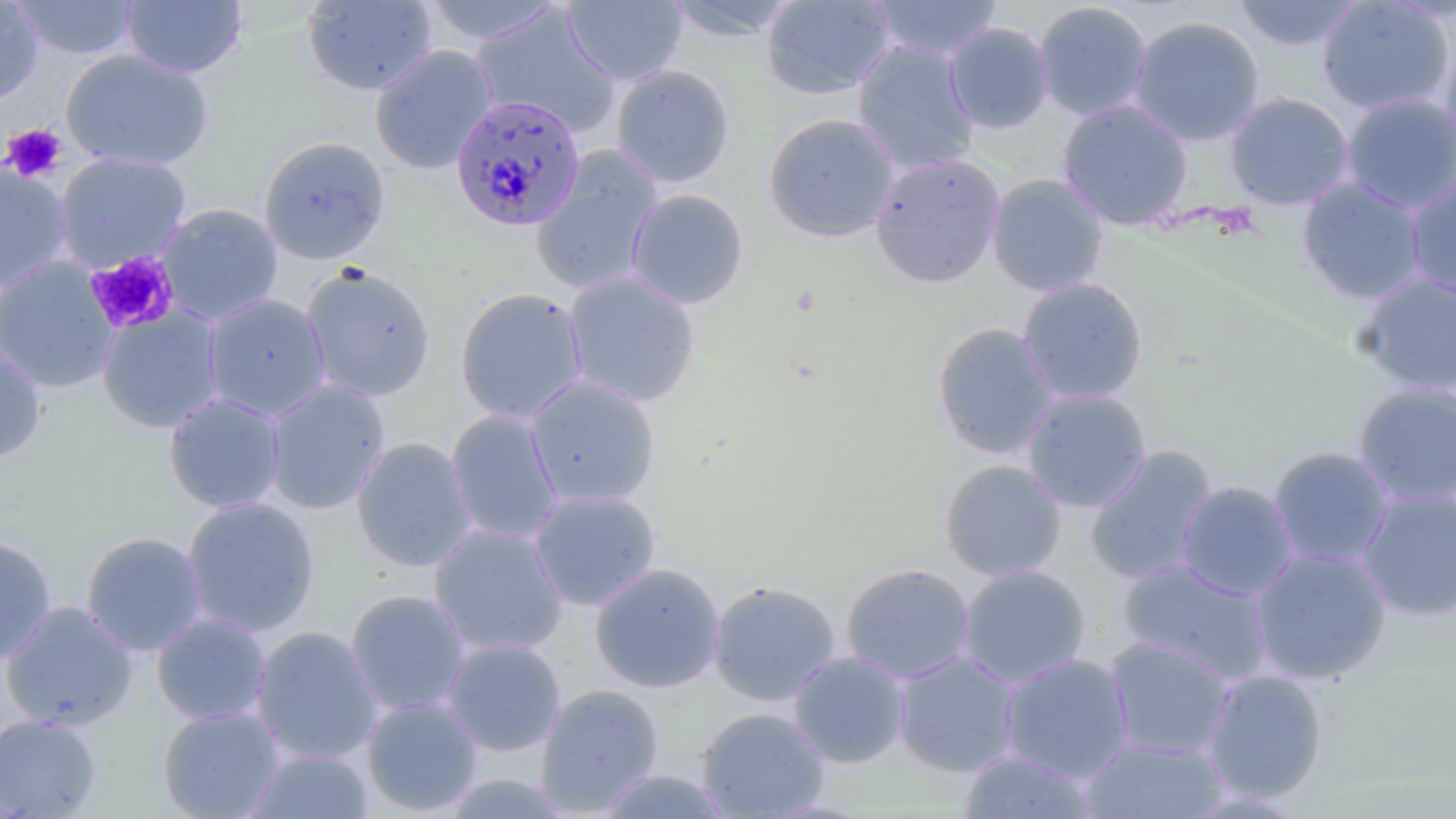 Approximate bounding boxes as (x1,y1)-(x2,y2) corner pairs in pixels. Uninfected red blood cell locations: (0,0)-(45,105), (10,0)-(141,61), (121,0)-(247,79), (301,0)-(438,96), (562,0)-(688,87), (662,0)-(802,43), (761,0)-(897,100), (867,0)-(1004,61), (1231,0)-(1366,52), (1316,0)-(1455,116), (421,1)-(564,45), (1033,1)-(1154,121), (470,6)-(620,139), (1128,15)-(1266,146), (943,21)-(1055,134), (852,39)-(980,175), (369,44)-(499,175), (1439,44)-(1456,164), (59,49)-(214,171), (610,64)-(735,188), (1224,91)-(1355,210), (1339,92)-(1456,214), (1057,98)-(1194,230), (763,112)-(900,243), (258,135)-(391,265), (530,147)-(664,297), (53,152)-(191,272), (869,152)-(1006,289), (0,160)-(73,295), (1404,173)-(1456,302), (986,174)-(1109,297), (1296,176)-(1428,305), (625,188)-(749,309), (157,203)-(284,325), (0,256)-(121,395), (300,264)-(436,402), (562,270)-(701,408), (1356,271)-(1456,396), (1017,277)-(1148,405), (454,287)-(589,425), (202,292)-(332,422), (95,305)-(225,434), (932,322)-(1059,461), (0,336)-(47,465), (524,374)-(661,509), (262,378)-(391,516), (1352,381)-(1456,507), (1021,387)-(1152,513), (162,392)-(286,514), (444,409)-(565,545), (351,436)-(478,572), (1084,445)-(1219,586), (1267,445)-(1395,569), (939,458)-(1067,582), (1176,480)-(1300,601), (1354,486)-(1455,621), (527,488)-(661,612), (180,496)-(320,638), (428,522)-(570,658), (80,531)-(208,656), (0,533)-(57,665), (1248,545)-(1393,685), (1117,558)-(1274,685), (589,562)-(726,693), (840,562)-(975,685), (957,564)-(1092,688), (707,579)-(841,706), (344,589)-(472,717), (0,601)-(139,732), (151,612)-(273,727), (249,625)-(383,765), (1104,635)-(1235,761), (441,637)-(566,757), (787,650)-(910,769), (893,650)-(1022,778), (998,651)-(1136,784), (1201,668)-(1329,804), (536,683)-(664,816), (361,695)-(484,816), (156,706)-(286,819), (695,706)-(831,818), (0,713)-(102,818), (1079,736)-(1231,818), (243,748)-(375,818), (958,749)-(1099,818), (593,768)-(735,818). Platelet locations: (1,124)-(67,183), (85,250)-(180,335). Plasmodium falciparum-infected red blood cell locations: (449,95)-(586,233). Slide-level diagnosis: Plasmodium falciparum. Thin blood smear. Optical microscopy. One field of a larger specimen. Image is 1456×819 pixels. Captured at 1000x magnification. May-Grünwald-Giemsa-stained preparation.